Identify the preparation type.
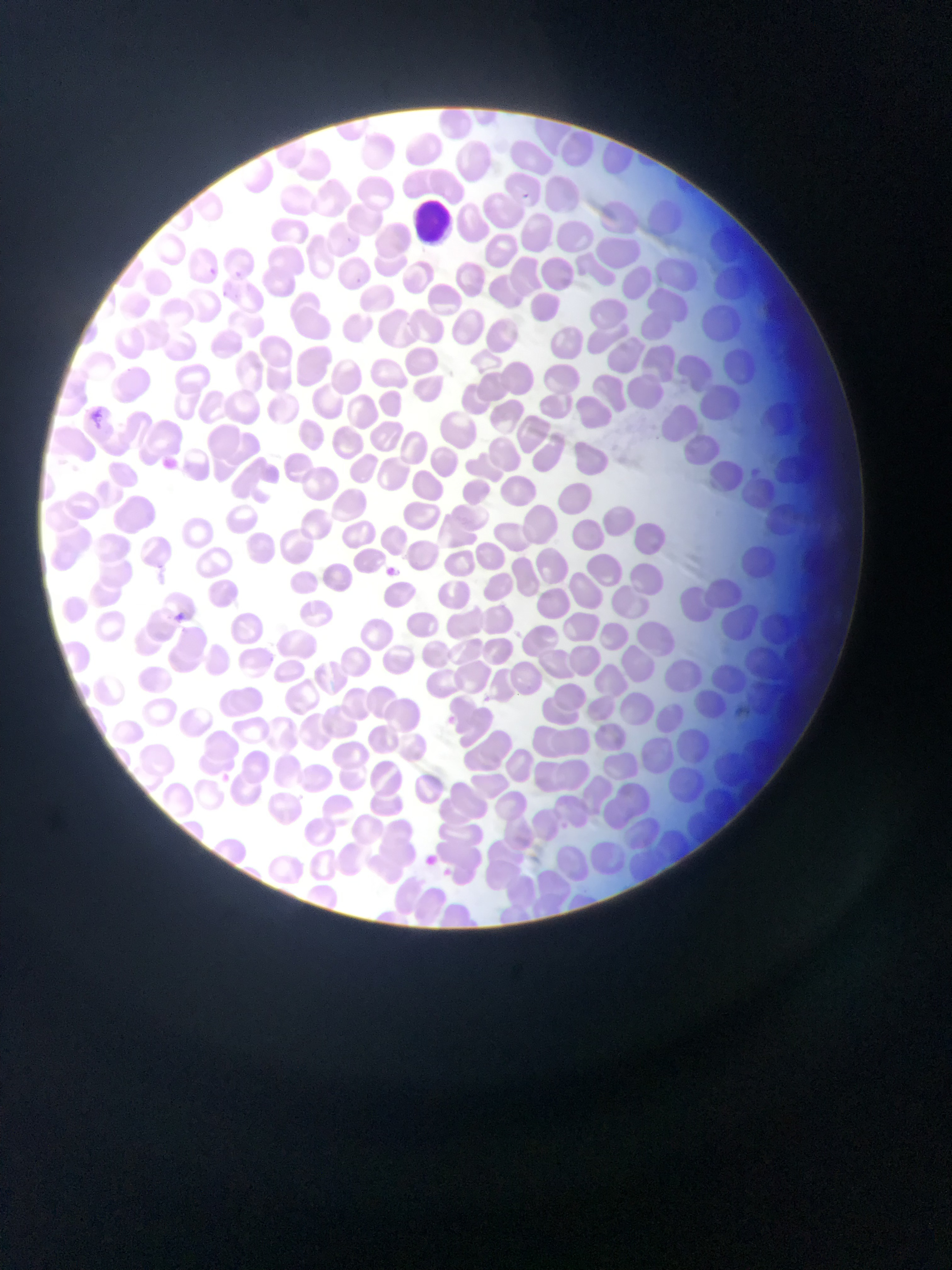
This is a thin smear.

Approximate bounding boxes as left top right bottom in pixels. Plasmodium parasite locations: 517 189 540 211; 342 236 354 246; 202 263 221 274; 231 266 246 282; 356 276 370 285; 87 405 104 427; 171 609 182 624; 439 714 458 731; 219 769 234 779; 422 847 444 870. Leukocyte locations: 408 202 454 252. Single field of view. Image is 952×1270 pixels. Photographed through a microscope with a mobile-phone camera. Sample from Ghana.